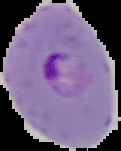

Summary:
  - Preparation: thin blood film
  - Image size: 121×151 pixels
  - Malaria status: parasitized
  - Image type: segmented cell region on a black background